Report the malaria status of this cell.
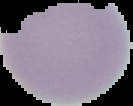
Uninfected.

preparation = thin blood smear
image size = 133×106 pixels
image type = segmented cell region on a black background